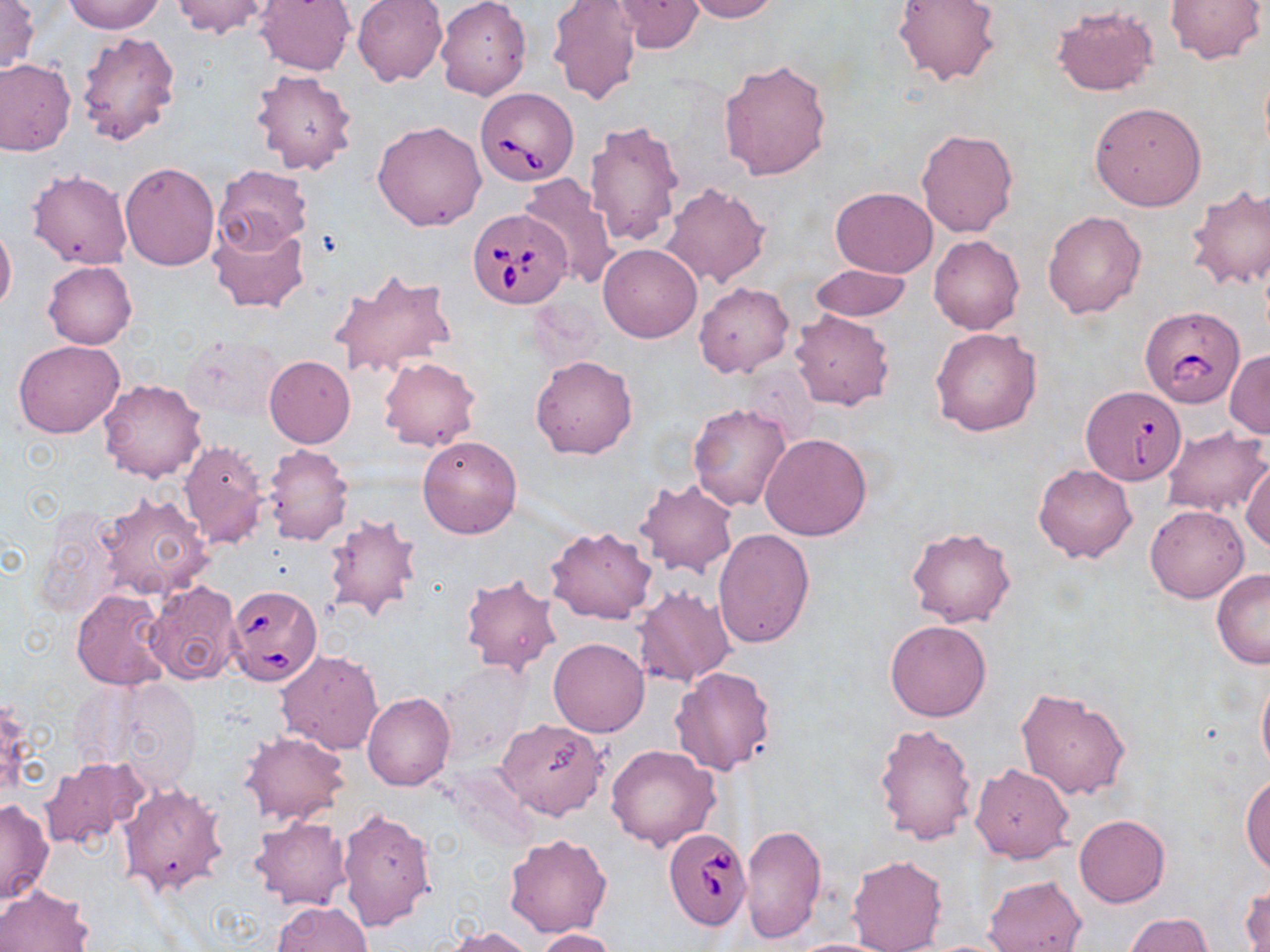

Summary:
  - Coordinate format: approximate bounding boxes as [x1, y1, x2, y2] in pixels
  - Uninfected red blood cell locations: [0, 0, 39, 74], [62, 0, 164, 33], [172, 0, 272, 39], [254, 0, 357, 76], [352, 0, 447, 86], [547, 0, 642, 105], [685, 0, 779, 22], [892, 0, 1001, 87], [1164, 0, 1265, 64], [435, 1, 531, 100], [613, 1, 705, 52], [1050, 4, 1159, 98], [77, 30, 181, 149], [718, 57, 831, 180], [0, 58, 75, 156], [251, 68, 357, 175], [1090, 102, 1206, 210], [584, 119, 684, 248], [372, 121, 487, 231], [916, 129, 1017, 238], [120, 162, 219, 270], [213, 165, 313, 252], [27, 170, 133, 269], [518, 174, 620, 290], [659, 181, 770, 288], [1185, 184, 1270, 291], [830, 187, 938, 278], [1042, 210, 1147, 319], [207, 215, 310, 315], [0, 221, 16, 316], [929, 235, 1025, 335], [598, 243, 702, 342], [44, 262, 136, 349], [811, 265, 911, 322], [330, 267, 457, 379], [693, 281, 793, 378], [790, 310, 894, 410], [930, 327, 1042, 436], [13, 339, 125, 438], [183, 340, 281, 421], [1226, 351, 1270, 438], [264, 355, 355, 447], [529, 355, 636, 460], [379, 357, 481, 452], [98, 379, 208, 483], [687, 402, 792, 511], [1161, 427, 1270, 516], [759, 433, 873, 541], [417, 434, 522, 539], [178, 440, 269, 549], [263, 443, 353, 546], [1242, 459, 1270, 553], [1033, 463, 1137, 563], [633, 479, 739, 579], [94, 492, 212, 603], [1144, 504, 1249, 602], [323, 515, 419, 622], [545, 525, 656, 625], [905, 525, 1017, 628], [712, 528, 815, 648], [1211, 568, 1270, 669], [459, 572, 563, 678], [145, 580, 241, 685], [633, 586, 736, 687], [71, 589, 169, 692], [885, 619, 991, 722], [549, 638, 649, 736], [276, 650, 384, 754], [438, 661, 531, 762], [670, 667, 776, 776], [1256, 668, 1270, 782], [108, 679, 205, 793], [1014, 687, 1130, 800], [362, 692, 455, 791], [495, 718, 608, 819], [875, 721, 978, 847], [241, 731, 349, 824], [605, 744, 720, 851], [39, 755, 151, 851], [970, 764, 1074, 863], [1241, 775, 1270, 874], [118, 779, 229, 895], [0, 797, 53, 906], [336, 806, 437, 933], [1074, 814, 1169, 907], [250, 816, 352, 911], [740, 823, 826, 948], [504, 834, 612, 937], [846, 853, 947, 952], [984, 876, 1087, 952], [0, 885, 93, 952], [1242, 885, 1269, 952], [272, 901, 373, 952], [1126, 913, 1215, 952], [442, 926, 534, 952], [535, 928, 617, 952], [782, 937, 897, 952]
  - Babesia divergens-infected red blood cell locations: [475, 87, 579, 186], [468, 208, 571, 309], [1138, 305, 1244, 412], [1081, 386, 1185, 489], [227, 585, 322, 685], [663, 827, 749, 929]
  - Slide-level diagnosis: Babesia divergens
  - Modality: optical microscopy
  - Magnification: 1000x
  - Image size: 1270×952 pixels
  - Stain: May-Grünwald-Giemsa
  - Field of view: one of a larger specimen
  - Preparation: thin blood smear